Report the malaria status.
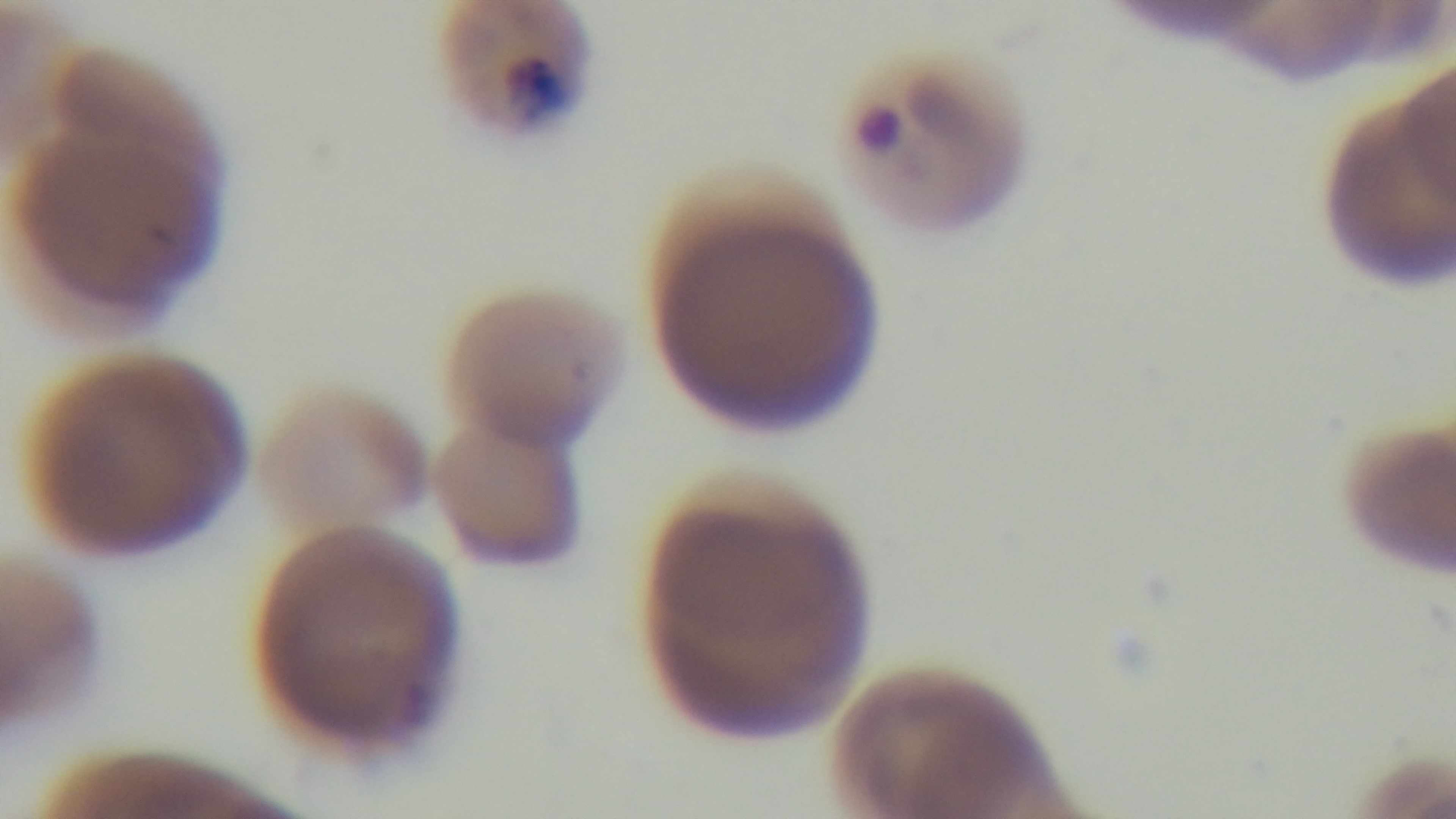

Infected.

capture = mounted 4K digital camera
objective = 100x oil immersion
field of view = single
preparation = thin smear
modality = light microscopy
stain = Giemsa